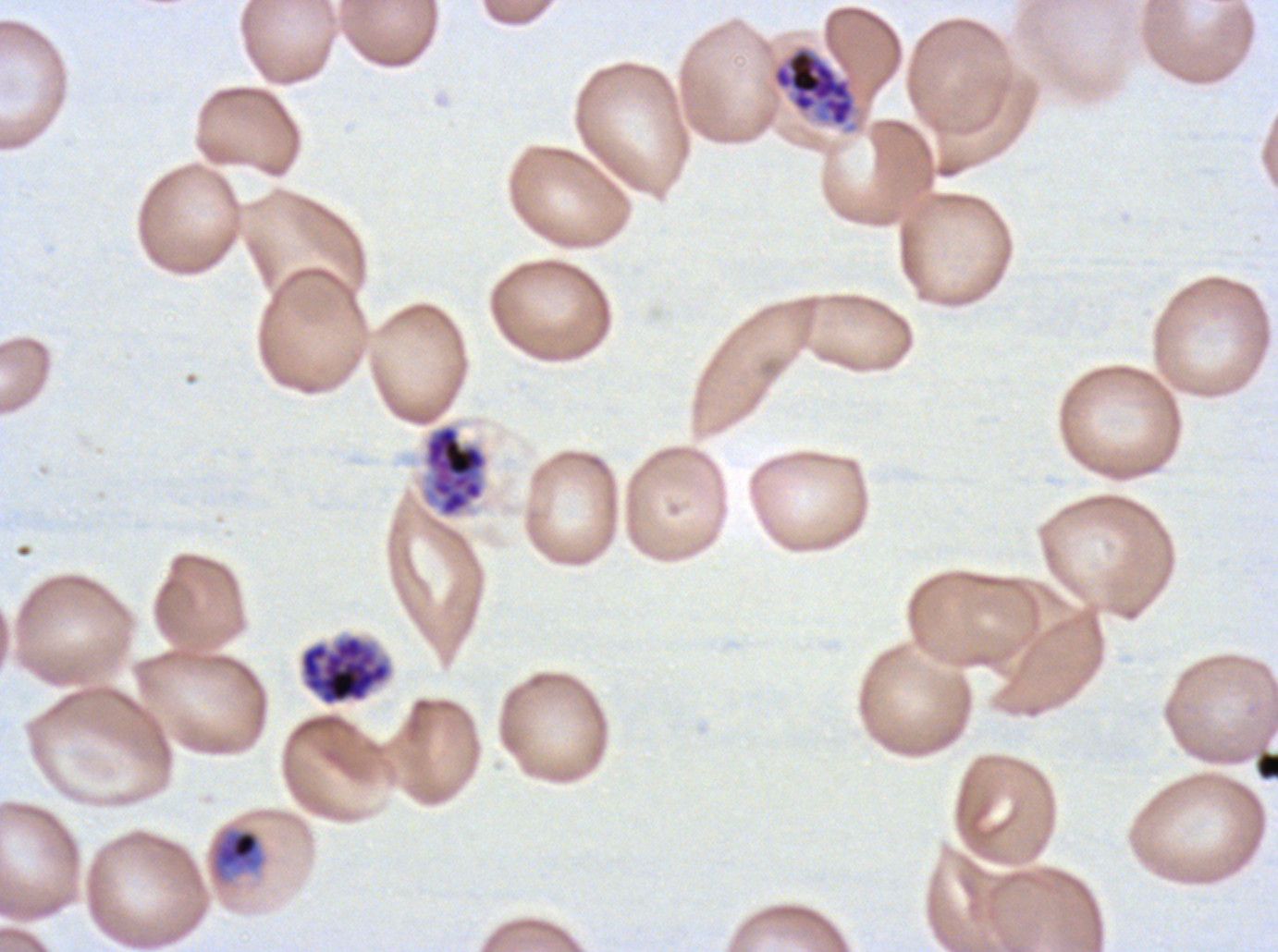

notation = approximate bounding boxes as {x1, y1, x2, y2} in pixels
late schizont locations = {771, 44, 857, 133}, {300, 635, 391, 705}
mid trophozoite locations = {212, 828, 263, 879}
segmenter locations = {421, 422, 489, 519}
debris locations = {1255, 751, 1277, 781}
preparation = thin blood film
image size = 1278×952 pixels
specimen = P. falciparum cultured ex vivo for 24 to 48 hours, from a patient in The Gambia
life-cycle stages observed = mid trophozoite, late schizont, segmenter
stain = Giemsa
field of view = sub-image separated from a larger composite